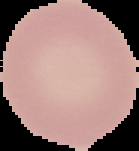
preparation = thin blood smear
malaria status = uninfected
image type = segmented cell region with the area outside set to black
image size = 139×151 pixels